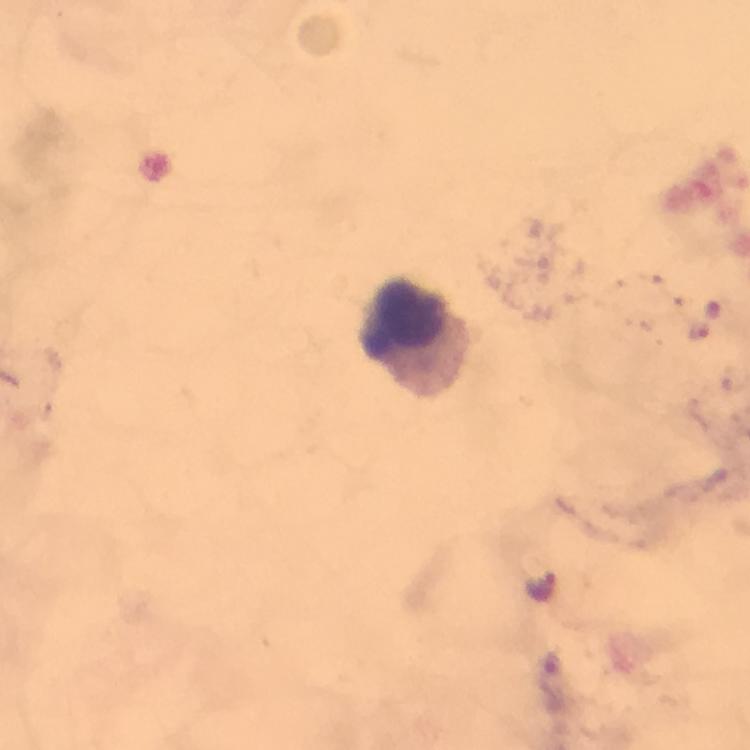
Approximate object centers, in pixels from the top-left corner. Plasmodium parasite locations: (x=699, y=330), (x=542, y=584). Leukocyte locations: (x=405, y=324). Image is 750×750 pixels. Immersion oil was used. 100x magnification. Smartphone photograph taken through a microscope. Cropped region of a single field of view. Thick smear. From a malaria diagnostic workup. Giemsa-stained preparation.